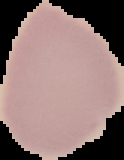

Summary:
  - Image type: segmented cell region on a black background
  - Preparation: thin blood smear
  - Result: no malaria parasites seen
  - Image size: 124×160 pixels